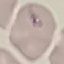
Malaria status: uninfected. Thin smear of blood. Cell patch, automatically extracted from a larger field of view and resized to 64 × 64 pixels. Giemsa-stained preparation. Acquired by smartphone through the microscope eyepiece.